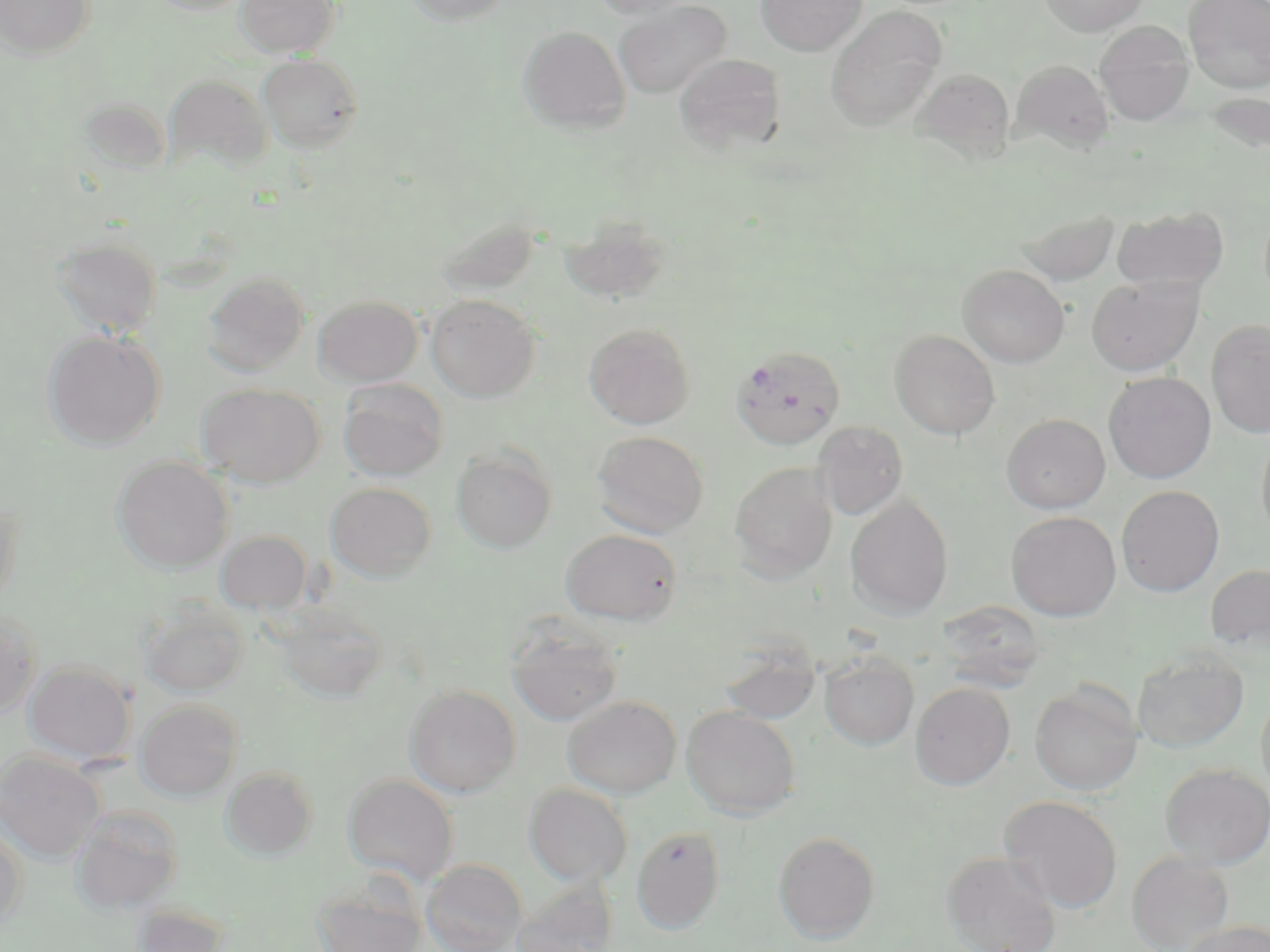
Summary:
  - Coordinate format: approximate bounding boxes as (x1, y1, x2, y2) in pixels
  - Plasmodium falciparum-infected red blood cell locations: (731, 345, 846, 449)
  - Uninfected red blood cell locations: (1, 0, 97, 60), (147, 0, 254, 16), (235, 0, 340, 58), (404, 0, 514, 25), (589, 0, 696, 20), (756, 0, 867, 56), (1039, 0, 1148, 36), (1183, 0, 1270, 92), (613, 1, 731, 99), (826, 5, 946, 132), (1095, 21, 1195, 124), (518, 26, 631, 134), (257, 53, 363, 153), (674, 53, 787, 155), (1010, 59, 1114, 153), (911, 68, 1015, 164), (164, 74, 273, 173), (1203, 92, 1270, 156), (76, 95, 169, 179), (1111, 207, 1229, 293), (1016, 209, 1121, 285), (434, 216, 541, 297), (560, 216, 673, 305), (52, 235, 162, 336), (958, 264, 1070, 367), (202, 271, 310, 376), (1086, 275, 1203, 376), (313, 294, 423, 387), (426, 294, 541, 402), (1205, 319, 1270, 437), (584, 322, 695, 429), (890, 329, 1000, 439), (42, 330, 165, 450), (1103, 371, 1216, 483), (338, 379, 449, 481), (196, 382, 324, 488), (1002, 413, 1110, 513), (813, 421, 908, 520), (591, 430, 710, 538), (1256, 430, 1270, 547), (451, 447, 557, 554), (112, 456, 234, 574), (730, 461, 837, 581), (325, 482, 436, 582), (1117, 485, 1224, 596), (0, 495, 23, 615), (846, 496, 953, 619), (1006, 511, 1121, 621), (561, 529, 682, 625), (215, 530, 312, 614), (1205, 563, 1270, 652), (137, 598, 250, 699), (936, 600, 1047, 689), (273, 603, 389, 705), (0, 606, 41, 718), (505, 616, 624, 726), (719, 636, 822, 725), (1132, 648, 1250, 753), (819, 652, 919, 750), (24, 660, 135, 765), (911, 681, 1015, 789), (1030, 681, 1143, 796), (404, 684, 521, 797), (1256, 688, 1270, 802), (562, 695, 681, 798), (135, 698, 244, 801), (681, 705, 801, 818), (0, 751, 105, 863), (1159, 763, 1270, 869), (220, 766, 319, 860), (343, 773, 458, 885), (524, 783, 633, 887), (999, 796, 1123, 913), (70, 805, 184, 915), (0, 824, 27, 928), (631, 826, 725, 934), (772, 831, 881, 943), (941, 850, 1062, 952), (1126, 852, 1236, 952), (421, 858, 527, 952), (313, 878, 428, 952), (512, 879, 619, 952), (130, 904, 231, 952), (1182, 920, 1270, 952)
  - Slide-level diagnosis: Plasmodium falciparum
  - Stain: May-Grünwald-Giemsa
  - Modality: optical microscopy
  - Magnification: 1000x
  - Preparation: thin blood smear
  - Image size: 1270×952 pixels
  - Field of view: single